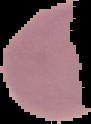
Summary:
  - Image type: segmented cell region with the area outside set to black
  - Image size: 91×124 pixels
  - Result: negative for malaria parasites
  - Preparation: thin blood film